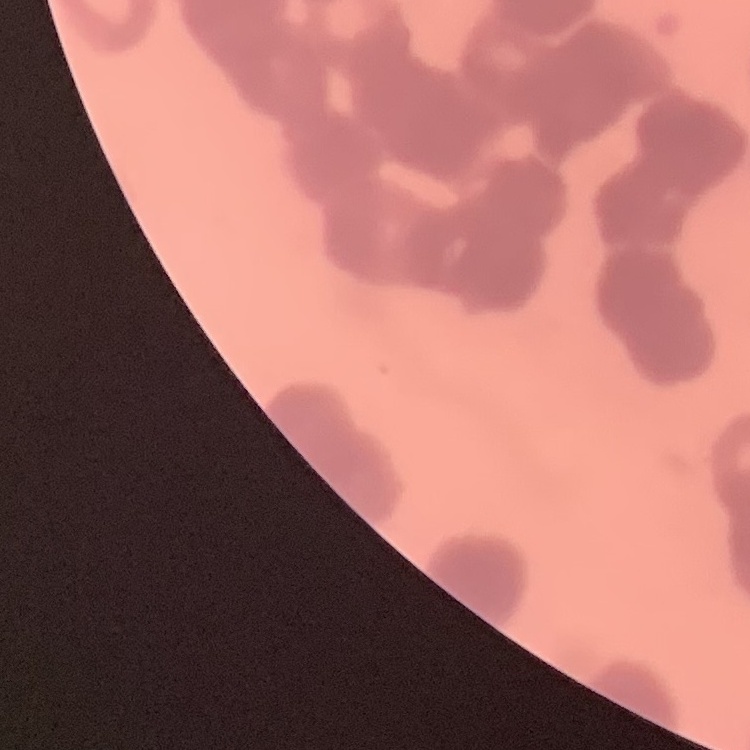

{
  "red_blood_cell_morphology": "rouleaux formation",
  "image_type": "square crop of a larger photomicrograph",
  "stain": "Field's or Giemsa",
  "preparation": "thin blood smear"
}